Name the parasite shown.
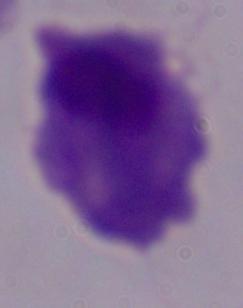
A trichomonad.

1000x magnification. Micrograph.